Locate every Plasmodium parasite and every leukocyte.
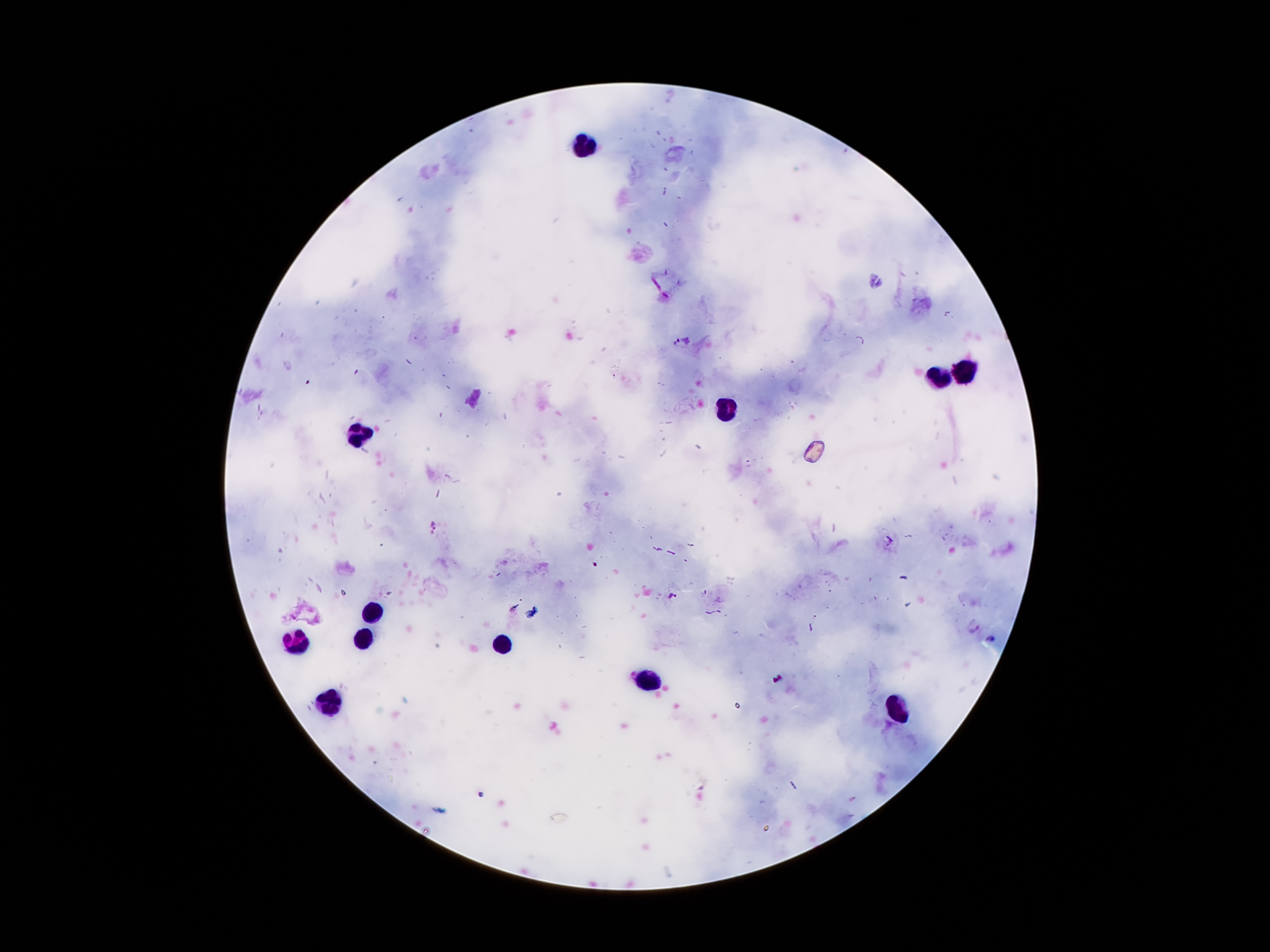
Approximate centers as {x, y} in pixels.
Plasmodium parasites: {682, 342}, {434, 523}, {672, 595}, {974, 626}, {991, 641}.
Leukocytes: {583, 144}, {963, 370}, {939, 381}, {728, 410}, {362, 437}, {375, 611}, {365, 639}, {297, 643}, {502, 645}, {647, 683}, {331, 704}, {898, 707}.

Summary:
  - Patient malaria status: infected with Plasmodium falciparum
  - Capture: smartphone through the microscope eyepiece
  - Stain: Giemsa
  - Field of view: one from this slide
  - Preparation: thick blood smear
  - Magnification: 100x
  - Image size: 1270×952 pixels